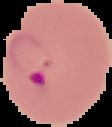
Summary:
  - Malaria status: parasitized
  - Image size: 112×127 pixels
  - Preparation: thin blood film
  - Image type: segmented cell region with the area outside set to black